Outline each Plasmodium falciparum-infected red blood cell.
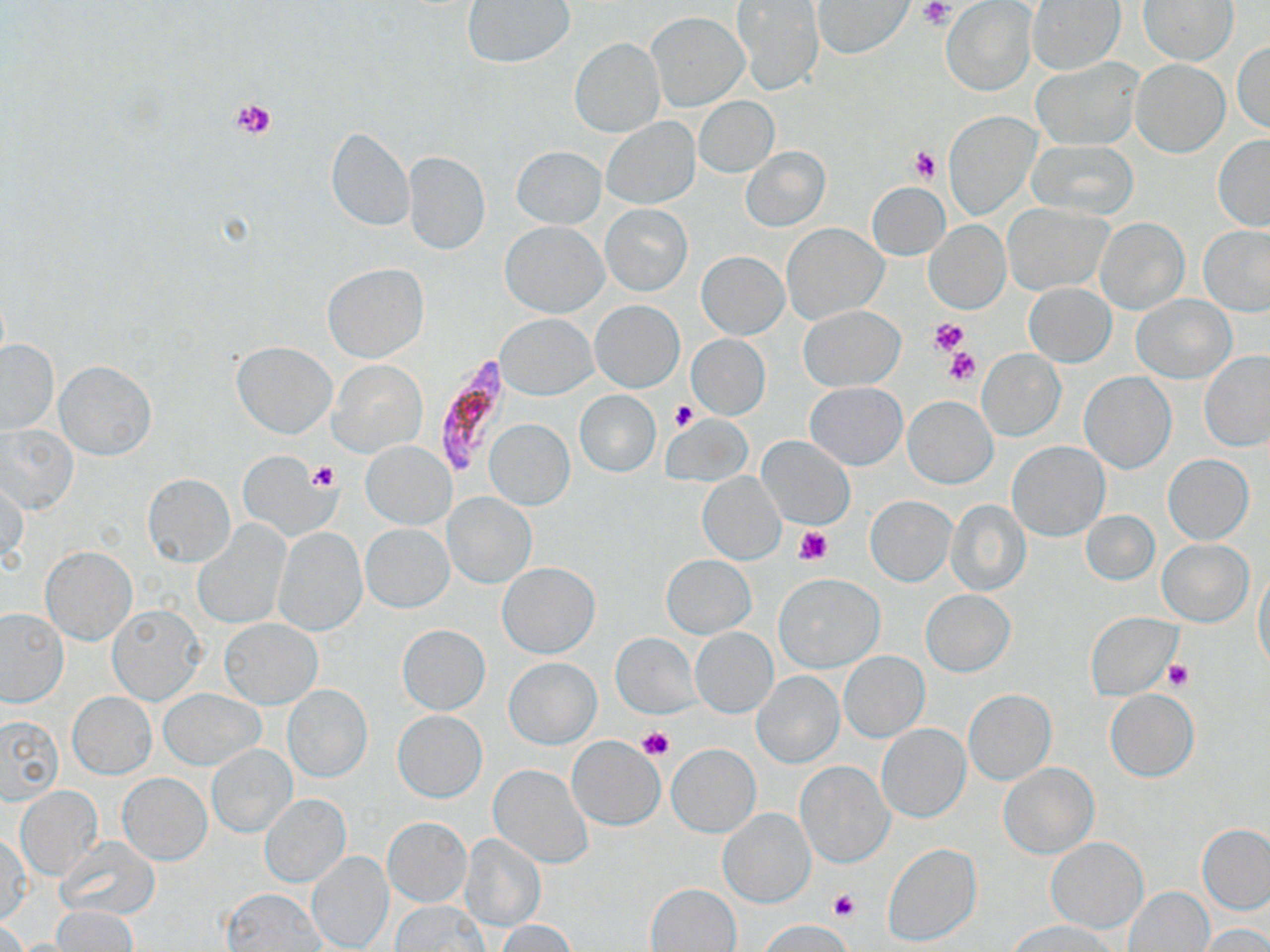

Approximate bounding boxes as [x1, y1, x2, y2] in pixels.
Plasmodium falciparum-infected red blood cells: [435, 356, 507, 472].

{
  "slide_level_diagnosis": "Plasmodium falciparum",
  "platelet_locations": "approximate bounding boxes as [x1, y1, x2, y2] in pixels: [917, 1, 956, 30], [230, 96, 278, 142], [909, 147, 941, 184], [929, 317, 970, 356], [944, 347, 979, 387], [670, 399, 701, 432], [308, 462, 338, 492], [792, 524, 833, 566], [1163, 661, 1193, 692], [636, 726, 673, 761], [828, 890, 861, 922], [772, 920, 848, 949]",
  "magnification": "1000x",
  "field_of_view": "one of a larger specimen",
  "image_size": "1270×952 pixels",
  "preparation": "thin blood film",
  "stain": "May-Grünwald-Giemsa",
  "modality": "optical microscopy",
  "uninfected_red_blood_cell_locations": "approximate bounding boxes as [x1, y1, x2, y2] in pixels: [1026, 0, 1124, 75], [1140, 0, 1238, 64], [463, 1, 575, 67], [812, 1, 912, 58], [942, 1, 1037, 96], [731, 2, 825, 95], [645, 11, 749, 112], [569, 38, 665, 137], [1233, 39, 1270, 134], [1031, 58, 1142, 151], [1131, 59, 1229, 156], [694, 97, 779, 176], [945, 112, 1038, 219], [601, 117, 700, 208], [325, 126, 414, 232], [1213, 135, 1270, 231], [1029, 138, 1139, 218], [739, 146, 830, 231], [512, 147, 605, 228], [403, 151, 490, 255], [867, 182, 949, 260], [1002, 203, 1110, 293], [601, 204, 691, 295], [1094, 217, 1189, 314], [924, 220, 1010, 314], [502, 222, 607, 318], [782, 223, 887, 325], [1199, 225, 1270, 317], [697, 251, 788, 339], [322, 263, 429, 363], [1025, 282, 1115, 365], [1133, 294, 1234, 381], [591, 300, 684, 391], [799, 305, 904, 389], [496, 314, 596, 398], [685, 334, 770, 420], [0, 339, 59, 434], [231, 340, 336, 439], [977, 350, 1065, 442], [1198, 351, 1270, 452], [328, 359, 427, 458], [55, 360, 155, 459], [1079, 372, 1177, 473], [805, 381, 907, 470], [575, 391, 660, 476], [902, 395, 996, 488], [485, 419, 573, 509], [0, 423, 79, 516], [759, 437, 854, 529], [361, 441, 455, 530], [1007, 441, 1109, 540], [238, 450, 335, 541], [1163, 455, 1254, 544], [698, 470, 784, 563], [142, 473, 235, 567], [1, 475, 27, 567], [443, 493, 535, 587], [866, 496, 955, 585], [944, 498, 1031, 596], [1082, 510, 1160, 585], [359, 522, 454, 612], [195, 524, 290, 630], [273, 527, 367, 635], [1156, 539, 1253, 627], [41, 547, 135, 645], [662, 554, 755, 638], [498, 562, 599, 658], [1253, 565, 1270, 673], [775, 574, 884, 672], [921, 590, 1015, 676], [107, 605, 205, 704], [0, 608, 67, 706], [1085, 612, 1180, 698], [219, 619, 321, 708], [397, 624, 490, 715], [691, 628, 777, 717], [612, 633, 700, 719], [839, 652, 929, 742], [505, 657, 600, 749], [751, 670, 844, 767], [283, 684, 372, 782], [159, 688, 265, 769], [964, 689, 1056, 784], [1105, 689, 1199, 781], [69, 692, 156, 777], [393, 710, 486, 802], [0, 715, 63, 803], [876, 723, 971, 823], [567, 735, 665, 830], [206, 744, 296, 837], [667, 744, 760, 837], [797, 760, 895, 868], [999, 763, 1098, 858], [490, 764, 591, 868], [118, 772, 210, 864], [16, 787, 101, 879], [261, 795, 351, 887], [719, 808, 815, 907], [384, 817, 471, 905], [1198, 824, 1270, 913], [1, 832, 32, 924], [460, 834, 545, 931], [58, 836, 159, 921], [1046, 837, 1148, 933], [882, 842, 982, 947], [307, 850, 394, 951], [646, 883, 740, 951], [1124, 886, 1213, 952], [223, 888, 324, 951], [392, 900, 488, 951], [50, 905, 138, 951], [758, 919, 853, 951], [497, 920, 580, 952], [1012, 921, 1114, 952], [1198, 925, 1270, 952]"
}